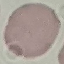

result = no malaria parasites seen
capture = smartphone camera at the microscope eyepiece
preparation = thin blood smear
stain = Giemsa
image type = cell patch, automatically extracted from a larger field of view and resized to 64 × 64 pixels